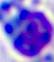
Summary:
  - Modality: micrograph
  - Identification: white blood cell
  - Magnification: 400x